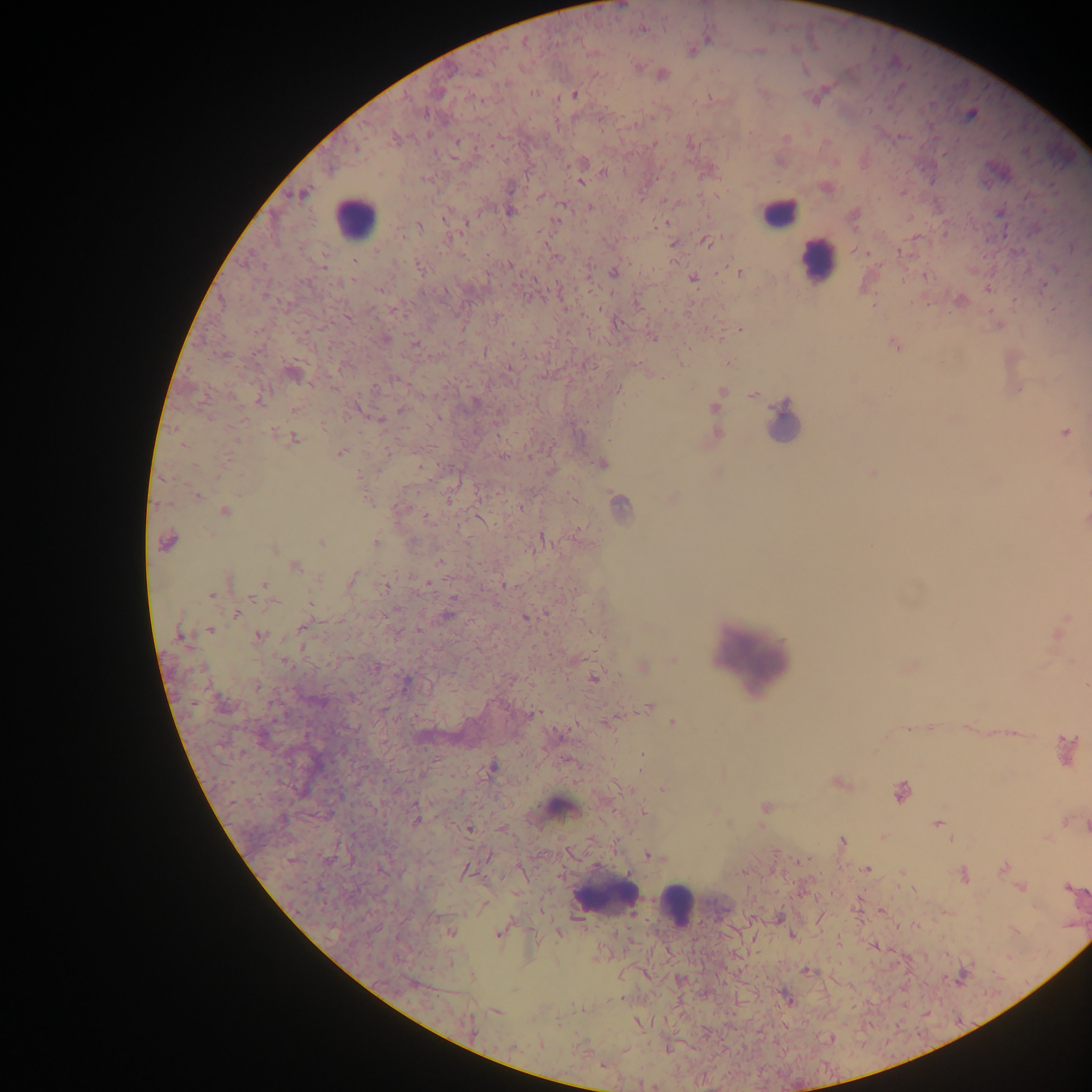
field of view = single
preparation = thick blood film
malaria parasite locations = approximate centers as (x, y) in pixels: (643, 29), (707, 39), (525, 42), (760, 50), (804, 71), (477, 72), (662, 74), (533, 93), (574, 95), (970, 115), (457, 142), (604, 171), (580, 182), (511, 188), (302, 195), (540, 196), (562, 207), (589, 208), (509, 211), (445, 218), (557, 220), (467, 223), (419, 227), (707, 242), (672, 244), (355, 261), (511, 266), (324, 267), (420, 268), (613, 272), (739, 272), (352, 279), (693, 279), (988, 288), (380, 290), (497, 317), (739, 329), (385, 338), (653, 338), (415, 343), (895, 345), (485, 351), (224, 355), (509, 369), (293, 375), (1018, 389), (720, 393), (753, 395), (260, 399), (474, 403), (714, 408), (402, 409), (295, 410), (378, 420), (273, 432), (1065, 432), (717, 433), (294, 439), (236, 441), (183, 444), (340, 453), (503, 457), (602, 464), (718, 473), (873, 473), (196, 496), (367, 499), (672, 499), (619, 503), (521, 507), (401, 509), (224, 512), (428, 517), (1086, 521), (542, 539), (321, 542), (375, 542), (167, 544), (274, 550), (439, 561), (294, 566), (319, 579), (353, 579), (426, 583), (264, 585), (506, 585), (385, 587), (211, 594), (252, 599), (274, 602), (310, 603), (236, 613), (449, 615), (525, 618), (301, 628), (210, 630), (419, 630), (259, 635), (179, 636), (673, 660), (283, 661), (643, 667), (375, 668), (593, 677), (1085, 685), (257, 686), (319, 702), (648, 707), (532, 715), (609, 722), (672, 722), (1067, 748), (642, 757), (492, 766), (838, 783), (663, 789), (901, 792), (764, 806), (643, 811), (417, 820), (938, 824), (470, 829), (842, 841), (487, 856), (652, 856), (1004, 867), (867, 869), (465, 871), (742, 872), (964, 876), (1020, 888), (1067, 888), (486, 904), (451, 933), (499, 933), (558, 935), (792, 935), (807, 972), (787, 998), (496, 1012), (468, 1022), (639, 1023), (603, 1065)
country = Ghana
image size = 1092×1092 pixels
capture = mobile-phone photograph through a microscope
leukocyte locations = approximate centers as (x, y) in pixels: (778, 213), (355, 220), (817, 260), (783, 419), (754, 654), (562, 807), (604, 895), (677, 906)